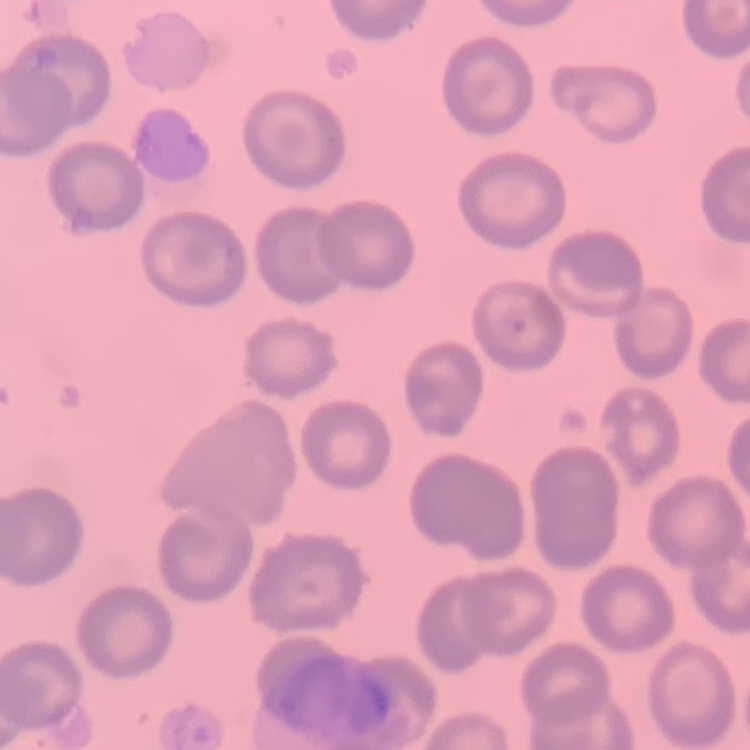

erythrocyte morphology = no rouleaux formation
image type = one tile cut from a larger photomicrograph
stain = Field's or Giemsa
preparation = thin peripheral smear